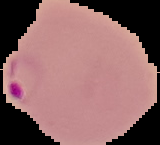
image size = 160×145 pixels
preparation = thin blood film
malaria status = parasitized
image type = segmented cell region on a black background